Give the extent of all Plasmodium falciparum-infected red blood cells.
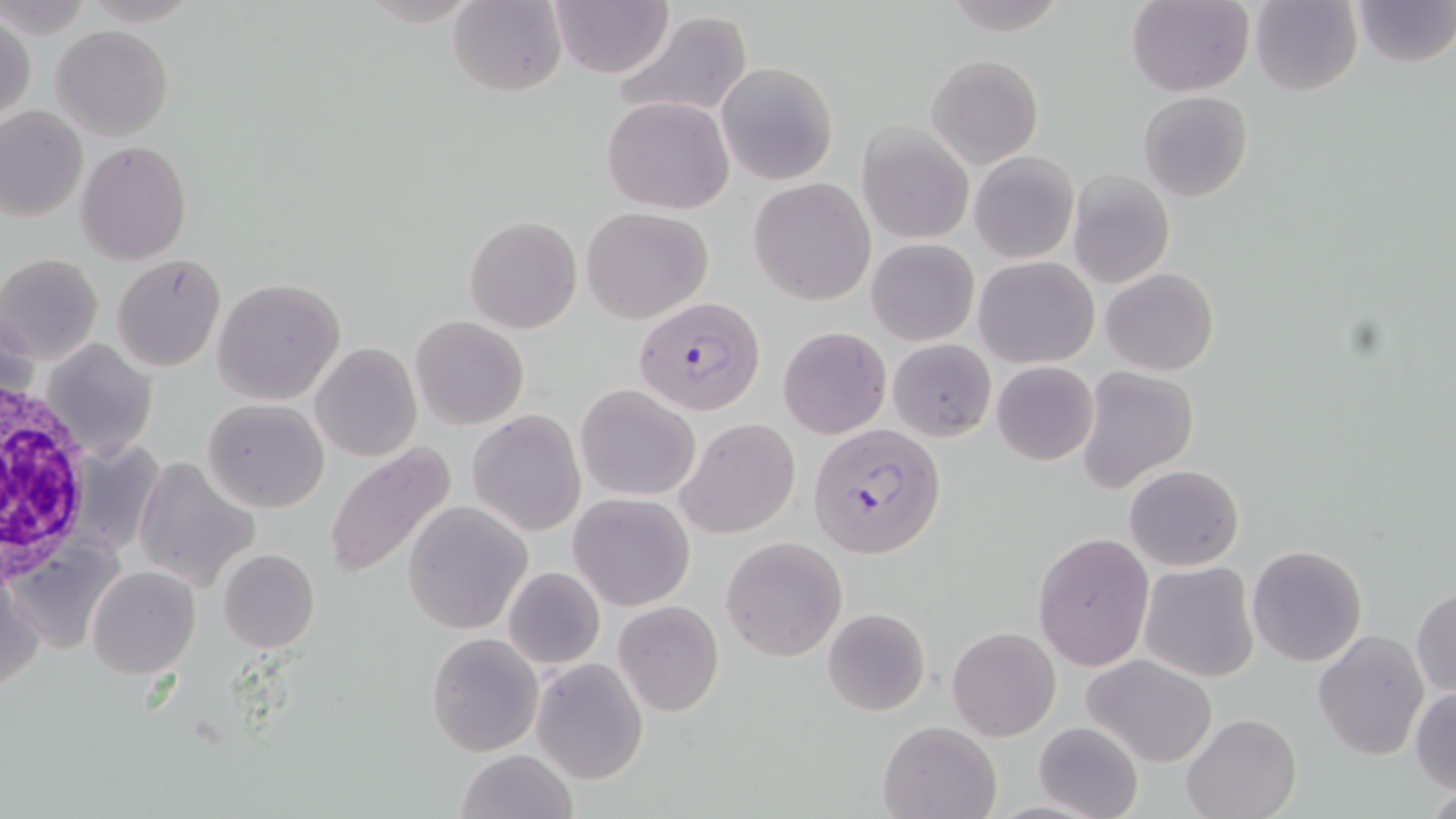
Approximate bounding boxes as [x1, y1, x2, y2] in pixels.
Plasmodium falciparum-infected red blood cells: [634, 296, 766, 415], [810, 422, 945, 558].

Summary:
  - Uninfected red blood cell locations: [448, 0, 566, 97], [548, 0, 674, 78], [1126, 0, 1254, 96], [1250, 0, 1362, 97], [1350, 0, 1455, 68], [612, 12, 752, 119], [1, 15, 35, 126], [53, 25, 173, 140], [926, 54, 1043, 170], [716, 62, 838, 185], [1137, 90, 1253, 202], [602, 96, 735, 213], [0, 106, 86, 220], [858, 124, 975, 245], [76, 141, 192, 263], [970, 152, 1079, 263], [1068, 169, 1174, 289], [749, 178, 875, 305], [581, 207, 713, 324], [464, 215, 581, 334], [867, 238, 978, 345], [0, 254, 104, 365], [111, 255, 227, 372], [975, 256, 1098, 368], [1102, 268, 1219, 375], [213, 278, 346, 404], [410, 315, 528, 430], [778, 327, 890, 439], [888, 338, 995, 440], [41, 339, 156, 460], [311, 343, 422, 462], [991, 361, 1099, 466], [1078, 367, 1198, 494], [576, 384, 701, 500], [202, 397, 330, 513], [468, 409, 585, 536], [675, 418, 801, 538], [322, 446, 457, 581], [134, 457, 259, 590], [1124, 464, 1244, 571], [568, 493, 694, 611], [402, 503, 531, 633], [1033, 531, 1154, 671], [722, 536, 847, 661], [7, 537, 124, 659], [1246, 544, 1367, 667], [218, 549, 320, 653], [1139, 562, 1259, 683], [503, 566, 605, 669], [86, 567, 199, 679], [0, 570, 43, 692], [1412, 586, 1455, 697], [613, 601, 724, 716], [822, 607, 931, 715], [947, 626, 1060, 741], [1313, 630, 1430, 760], [426, 632, 541, 756], [1085, 654, 1218, 767], [532, 658, 648, 785], [1410, 687, 1456, 795], [1182, 714, 1300, 819], [877, 720, 1004, 818], [1032, 721, 1145, 819], [455, 749, 579, 819]
  - White blood cell locations: [0, 376, 93, 583]
  - Slide-level diagnosis: Plasmodium falciparum
  - Modality: optical microscopy
  - Magnification: 1000x
  - Preparation: thin blood smear
  - Field of view: one of a larger specimen
  - Image size: 1456×819 pixels
  - Stain: May-Grünwald-Giemsa